Name the parasite shown.
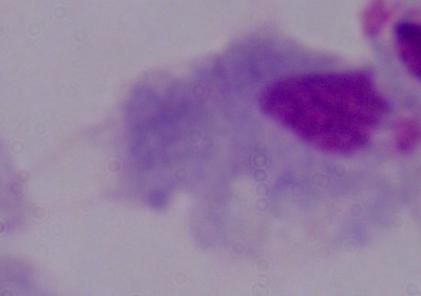
This is a trichomonad.

Photomicrograph. Captured at 1000x magnification.